State which parasite is depicted.
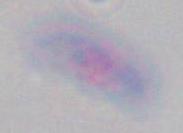

This is Toxoplasma gondii.

Summary:
  - Magnification: 1000x
  - Modality: photomicrograph